State which cell type is depicted.
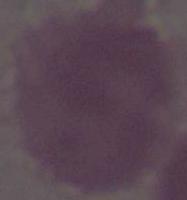
An erythrocyte.

Summary:
  - Magnification: 1000x
  - Modality: micrograph